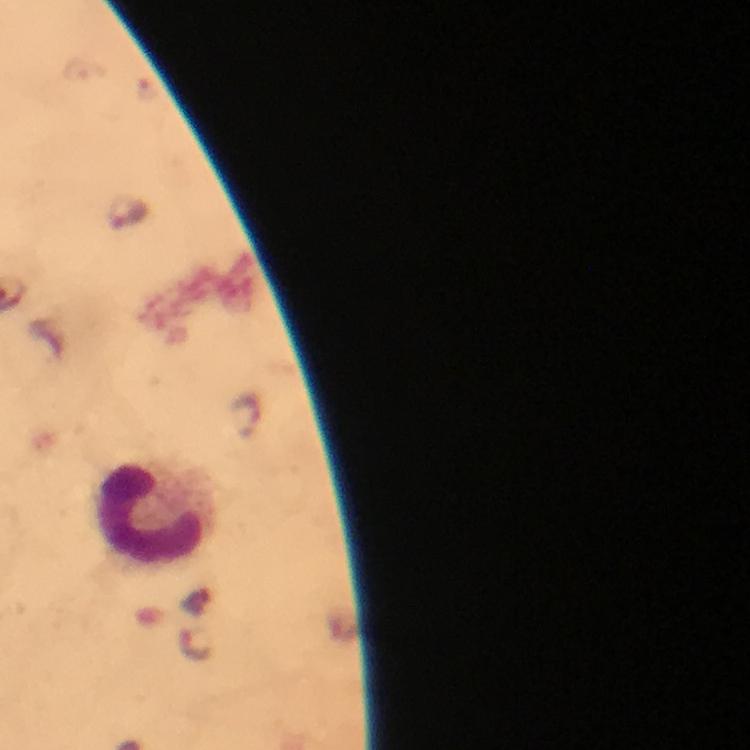 Approximate object centers, in pixels from the top-left corner. Leukocyte locations: (x=151, y=517). Malaria parasite locations: (x=197, y=643). Giemsa-stained preparation. Photographed through the microscope with a smartphone camera. A crop from one field of view. At 100x magnification. Immersion oil applied. Image is 750×750 pixels. From a malaria diagnostic workup. Thick blood smear.